Locate every uninfected red blood cell.
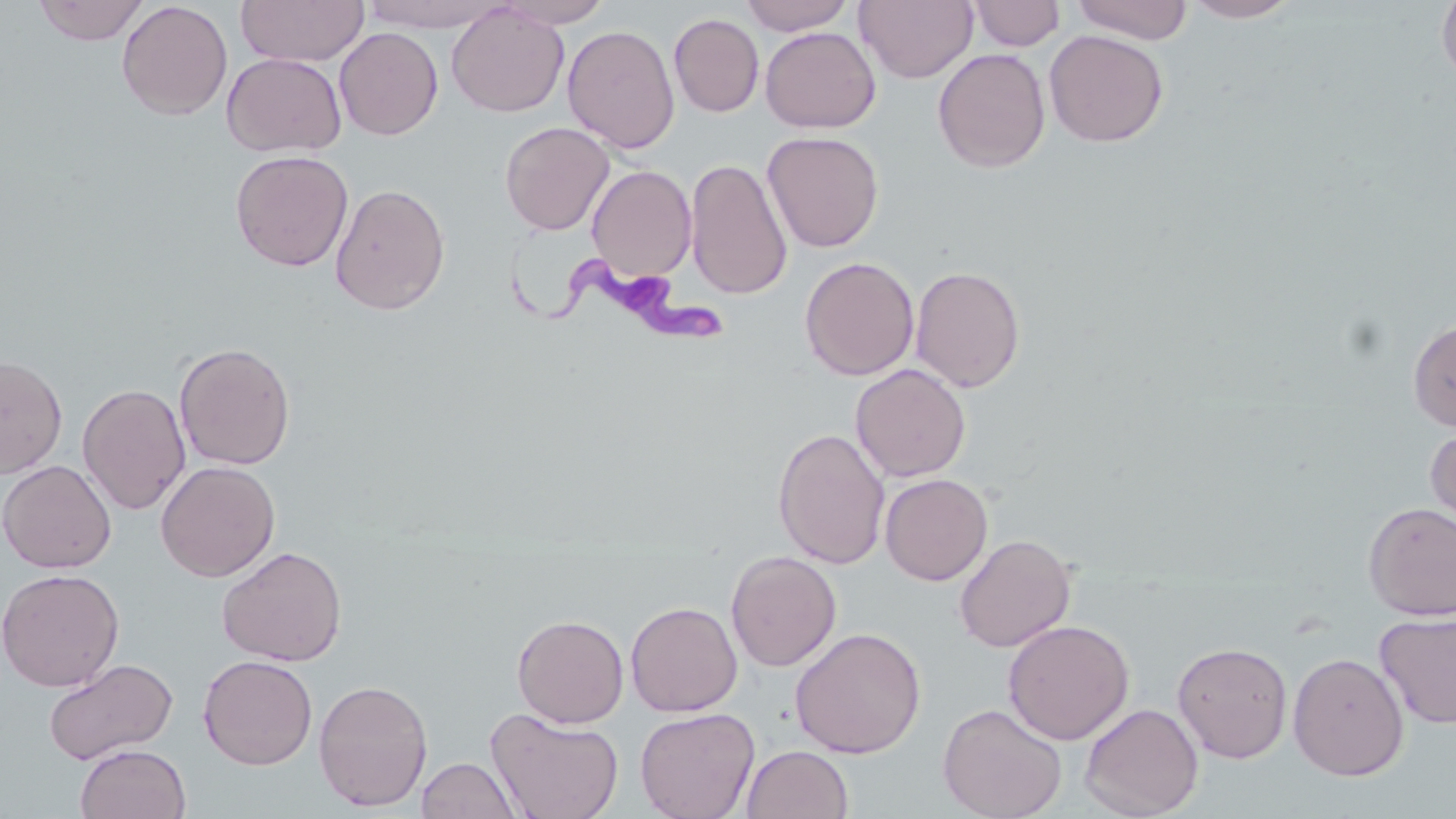
Approximate bounding boxes as named x1/y1/x2/y2 corners in pixels.
Uninfected red blood cells: (x1=33, y1=0, x2=149, y2=45), (x1=235, y1=0, x2=369, y2=66), (x1=359, y1=0, x2=512, y2=33), (x1=495, y1=0, x2=614, y2=28), (x1=738, y1=0, x2=856, y2=35), (x1=967, y1=0, x2=1065, y2=51), (x1=1070, y1=0, x2=1193, y2=44), (x1=1181, y1=0, x2=1303, y2=22), (x1=1436, y1=0, x2=1456, y2=87), (x1=117, y1=1, x2=233, y2=120), (x1=854, y1=1, x2=978, y2=84), (x1=446, y1=3, x2=569, y2=118), (x1=669, y1=13, x2=764, y2=117), (x1=562, y1=25, x2=680, y2=154), (x1=760, y1=26, x2=880, y2=132), (x1=334, y1=27, x2=443, y2=140), (x1=1044, y1=29, x2=1169, y2=147), (x1=931, y1=44, x2=1167, y2=158), (x1=933, y1=48, x2=1051, y2=173), (x1=222, y1=52, x2=346, y2=157), (x1=499, y1=121, x2=615, y2=235), (x1=762, y1=131, x2=884, y2=253), (x1=230, y1=150, x2=354, y2=271), (x1=685, y1=158, x2=792, y2=301), (x1=586, y1=164, x2=697, y2=281), (x1=330, y1=182, x2=450, y2=315), (x1=799, y1=256, x2=919, y2=381), (x1=910, y1=265, x2=1027, y2=393), (x1=1408, y1=318, x2=1456, y2=432), (x1=174, y1=341, x2=296, y2=470), (x1=0, y1=354, x2=68, y2=478), (x1=850, y1=363, x2=971, y2=482), (x1=77, y1=383, x2=191, y2=515), (x1=1424, y1=424, x2=1456, y2=539), (x1=773, y1=427, x2=890, y2=570), (x1=0, y1=460, x2=116, y2=573), (x1=156, y1=460, x2=280, y2=581), (x1=880, y1=473, x2=992, y2=585), (x1=1362, y1=502, x2=1456, y2=620), (x1=954, y1=533, x2=1076, y2=652), (x1=217, y1=545, x2=347, y2=666), (x1=726, y1=550, x2=842, y2=671), (x1=0, y1=568, x2=124, y2=691), (x1=626, y1=601, x2=742, y2=716), (x1=1374, y1=610, x2=1456, y2=729), (x1=512, y1=613, x2=629, y2=728), (x1=1003, y1=619, x2=1135, y2=745), (x1=789, y1=626, x2=927, y2=759), (x1=1172, y1=641, x2=1293, y2=763), (x1=1288, y1=652, x2=1410, y2=781), (x1=198, y1=655, x2=318, y2=770), (x1=43, y1=658, x2=178, y2=766), (x1=313, y1=678, x2=433, y2=811), (x1=937, y1=702, x2=1067, y2=819), (x1=1080, y1=702, x2=1204, y2=818), (x1=485, y1=707, x2=625, y2=819), (x1=635, y1=707, x2=760, y2=819), (x1=75, y1=744, x2=191, y2=819), (x1=741, y1=745, x2=854, y2=819), (x1=417, y1=756, x2=522, y2=818).

Summary:
  - Trypanosoma brucei locations: (x1=497, y1=238, x2=732, y2=352)
  - Slide-level diagnosis: Trypanosoma brucei
  - Modality: light microscopy
  - Magnification: 1000x
  - Field of view: one of a larger specimen
  - Stain: May-Grünwald-Giemsa
  - Preparation: thin blood film
  - Image size: 1456×819 pixels